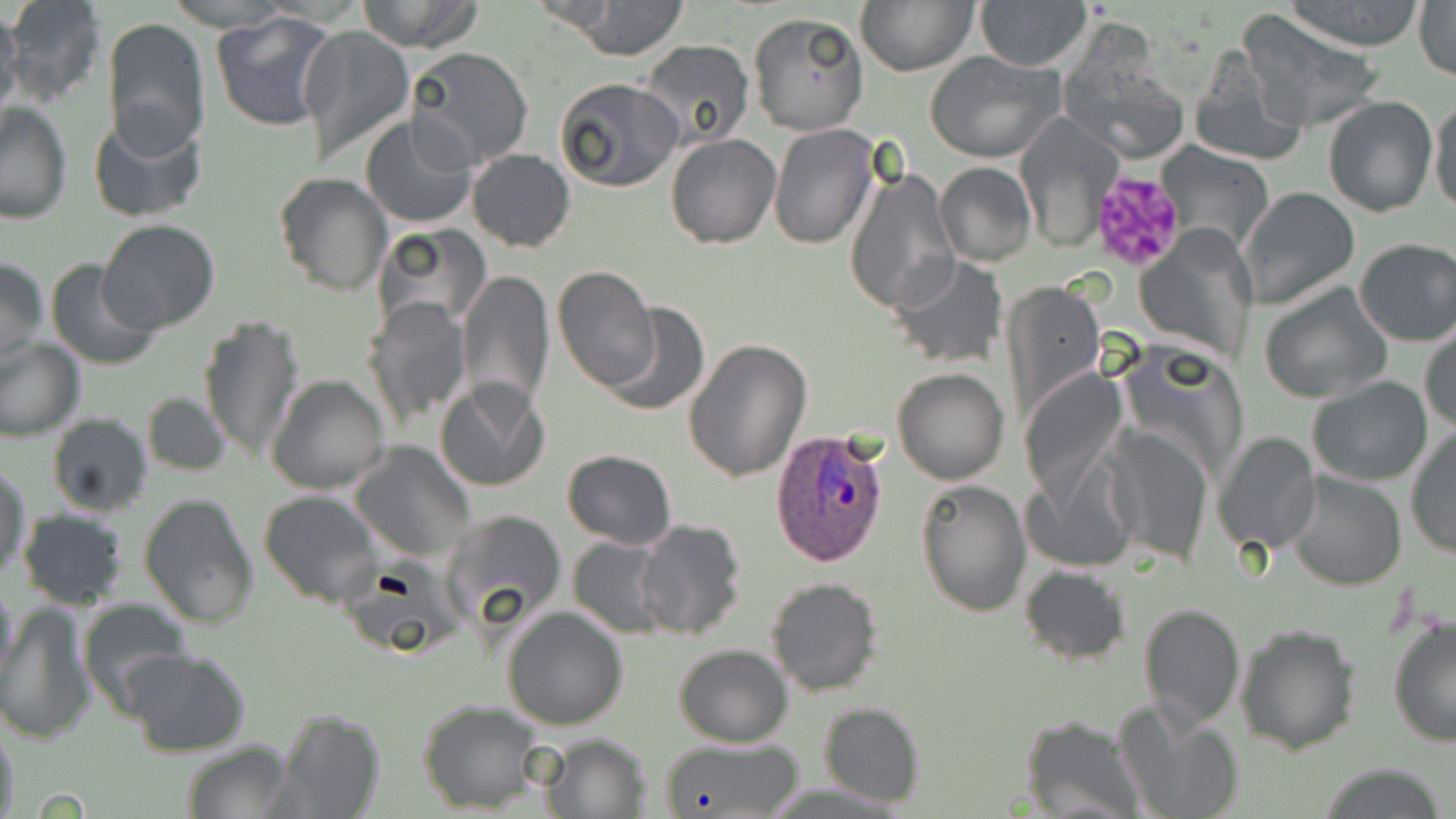
slide-level diagnosis = Plasmodium ovale
preparation = thin blood film
Plasmodium ovale-infected red blood cell locations = approximate bounding boxes as (x1,y1)-(x2,y2) corner pairs in pixels: (771,429)-(889,568)
modality = optical microscopy
platelet locations = approximate bounding boxes as (x1,y1)-(x2,y2) corner pairs in pixels: (1089,170)-(1187,273)
magnification = 1000x
field of view = one of a larger specimen
stain = May-Grünwald-Giemsa
uninfected red blood cell locations = approximate bounding boxes as (x1,y1)-(x2,y2) corner pairs in pixels: (2,0)-(107,109), (157,0)-(303,32), (355,0)-(487,53), (567,0)-(690,60), (855,0)-(978,75), (1284,0)-(1427,50), (0,2)-(22,121), (975,2)-(1092,71), (1413,2)-(1456,78), (211,8)-(341,132), (1235,8)-(1385,132), (748,13)-(868,135), (102,17)-(211,153), (296,24)-(415,167), (638,39)-(755,152), (1189,45)-(1309,168), (404,46)-(534,171), (1060,48)-(1190,164), (926,50)-(1064,163), (554,77)-(685,193), (1322,97)-(1438,217), (1430,97)-(1455,220), (1,102)-(74,224), (88,111)-(208,224), (1014,114)-(1121,248), (359,115)-(479,232), (769,125)-(877,249), (299,129)-(428,288), (665,133)-(781,249), (1157,142)-(1276,256), (466,148)-(576,251), (935,161)-(1035,266), (845,164)-(959,315), (275,173)-(392,296), (1241,187)-(1360,310), (98,218)-(221,333), (370,224)-(492,334), (1138,227)-(1253,360), (1353,237)-(1456,345), (413,239)-(536,383), (890,254)-(1008,368), (0,256)-(48,366), (44,257)-(163,371), (553,265)-(660,392), (456,269)-(554,413), (1002,278)-(1106,430), (1259,282)-(1393,405), (362,295)-(471,427), (600,303)-(709,417), (197,312)-(306,466), (1420,327)-(1455,435), (0,336)-(84,441), (684,338)-(812,483), (893,367)-(1009,484), (1020,371)-(1133,498), (267,374)-(389,494), (1308,377)-(1433,488), (435,378)-(552,493), (143,391)-(230,476), (46,413)-(154,519), (1103,424)-(1213,564), (1406,428)-(1455,557), (1212,432)-(1320,555), (349,441)-(476,563), (1021,448)-(1140,571), (561,449)-(676,550), (0,465)-(32,580), (1285,472)-(1406,590), (915,478)-(1031,617), (259,489)-(384,607), (138,492)-(259,630), (16,507)-(130,610), (438,507)-(568,639), (635,518)-(748,642), (569,536)-(676,638), (1019,565)-(1131,666), (765,575)-(884,696), (0,581)-(20,695), (77,597)-(193,718), (1,601)-(96,745), (1138,603)-(1246,731), (502,607)-(629,730), (1386,612)-(1456,747), (1236,623)-(1362,753), (673,644)-(793,746), (123,647)-(250,758), (1117,697)-(1245,819), (418,700)-(542,813), (818,702)-(926,809), (272,707)-(384,819), (1019,716)-(1145,817), (0,722)-(20,819), (540,732)-(650,817), (654,737)-(805,818), (180,741)-(294,819), (1317,765)-(1450,819)
image size = 1456×819 pixels